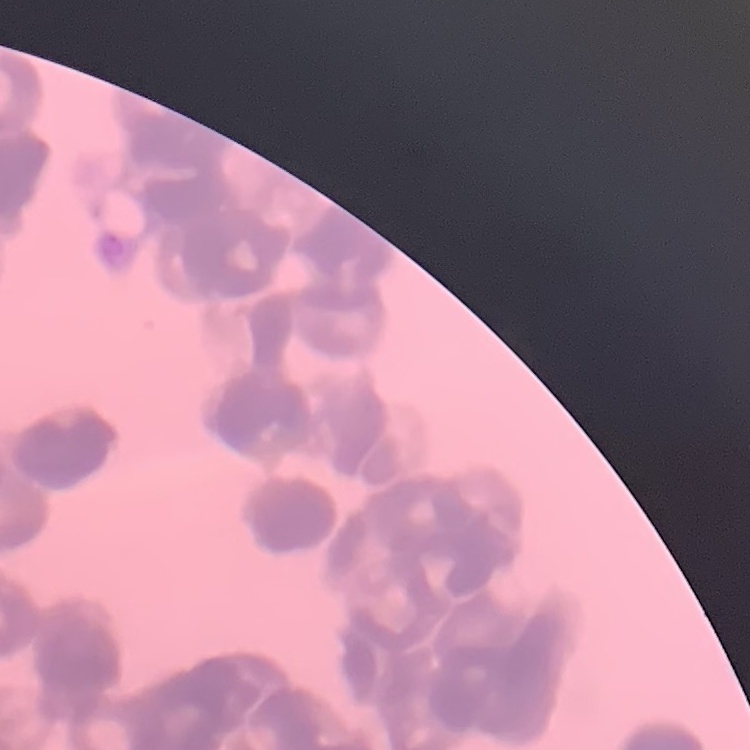
The erythrocytes exhibit rouleaux formation. One tile cut from a larger photomicrograph. Field's or Giemsa stain. Thin peripheral smear.